Assess for malaria.
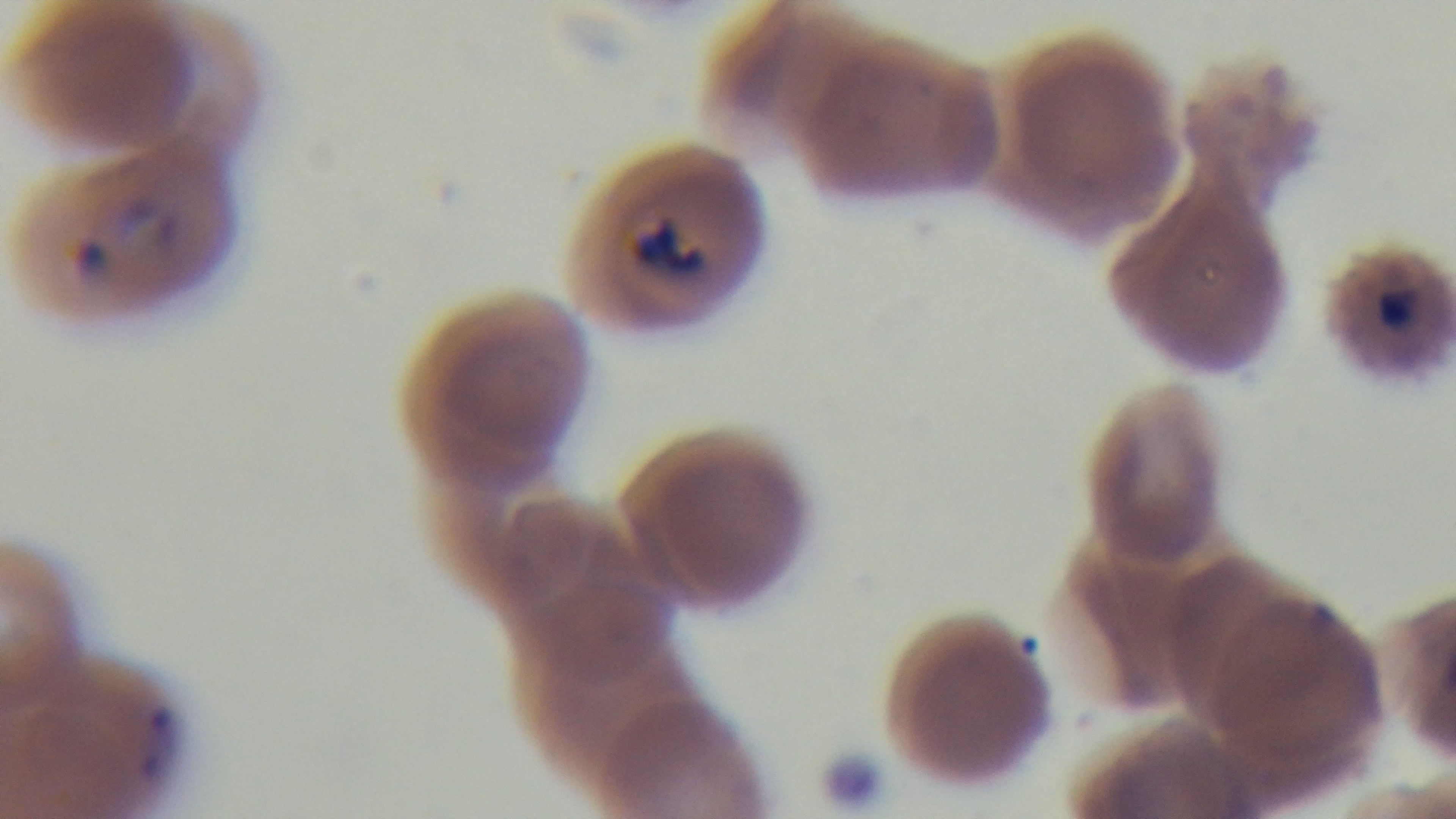
It is infected.

stain = Giemsa
field of view = one from the slide
preparation = thin smear
capture = mounted 4K digital camera
objective = 100x oil immersion
modality = light microscopy